Comment on the morphology of the red blood cells.
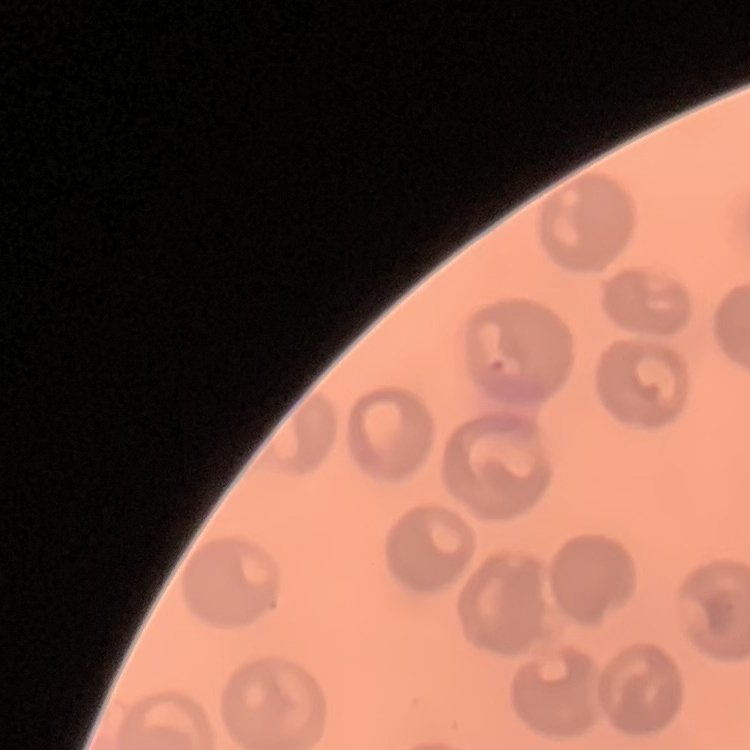
They show no rouleaux formation.

Summary:
  - Preparation: thin peripheral smear
  - Image type: one tile cut from a larger photomicrograph
  - Stain: Field's or Giemsa